Assess this cell for malaria.
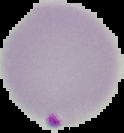

Parasitized.

{
  "preparation": "thin blood smear",
  "image_type": "cell region segmented out of the field of view; surrounding area masked to black",
  "image_size": "124×133 pixels"
}